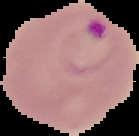 From a thin blood smear. Segmented cell region on a black background. Image is 139×136 pixels. Result: malaria parasites identified.